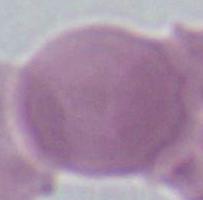
Captured at 1000x magnification. An erythrocyte is shown. Micrograph.